Comment on the morphology of the erythrocytes.
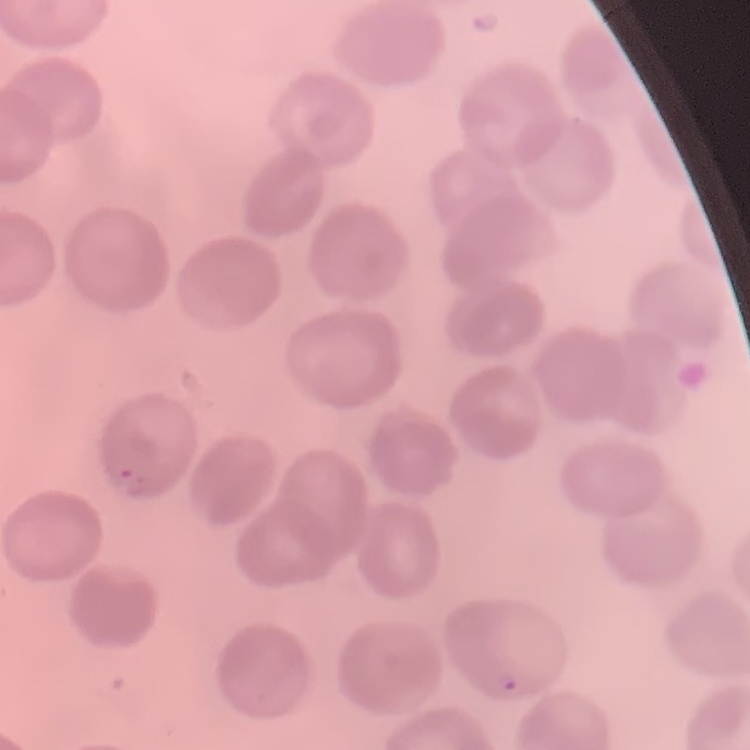
They show no rouleaux formation.

preparation = thin blood smear
stain = Field's or Giemsa
image type = one tile cut from a larger photomicrograph